Comment on the morphology of the red blood cells.
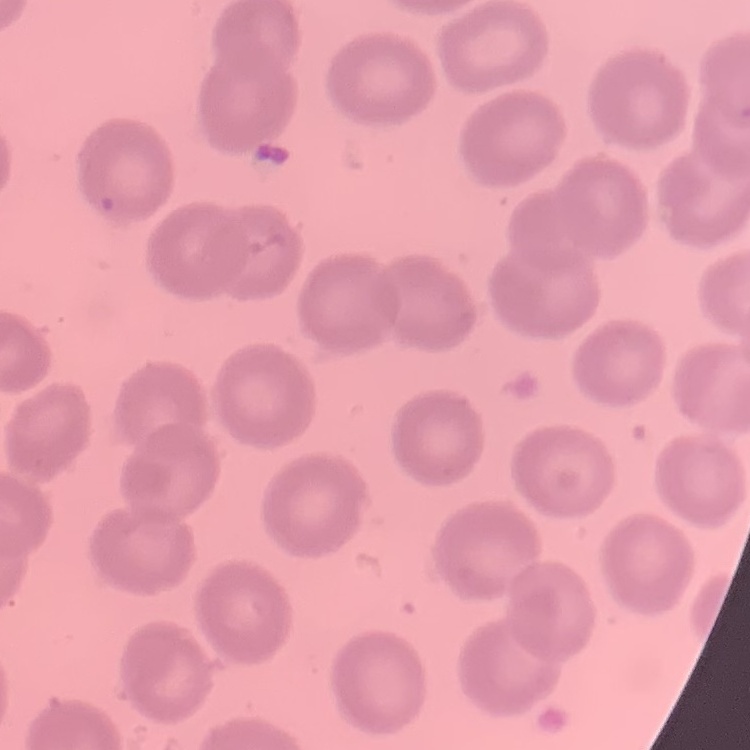
No rouleaux formation.

Summary:
  - Preparation: thin peripheral smear
  - Image type: square crop of a larger photomicrograph
  - Stain: Field's or Giemsa